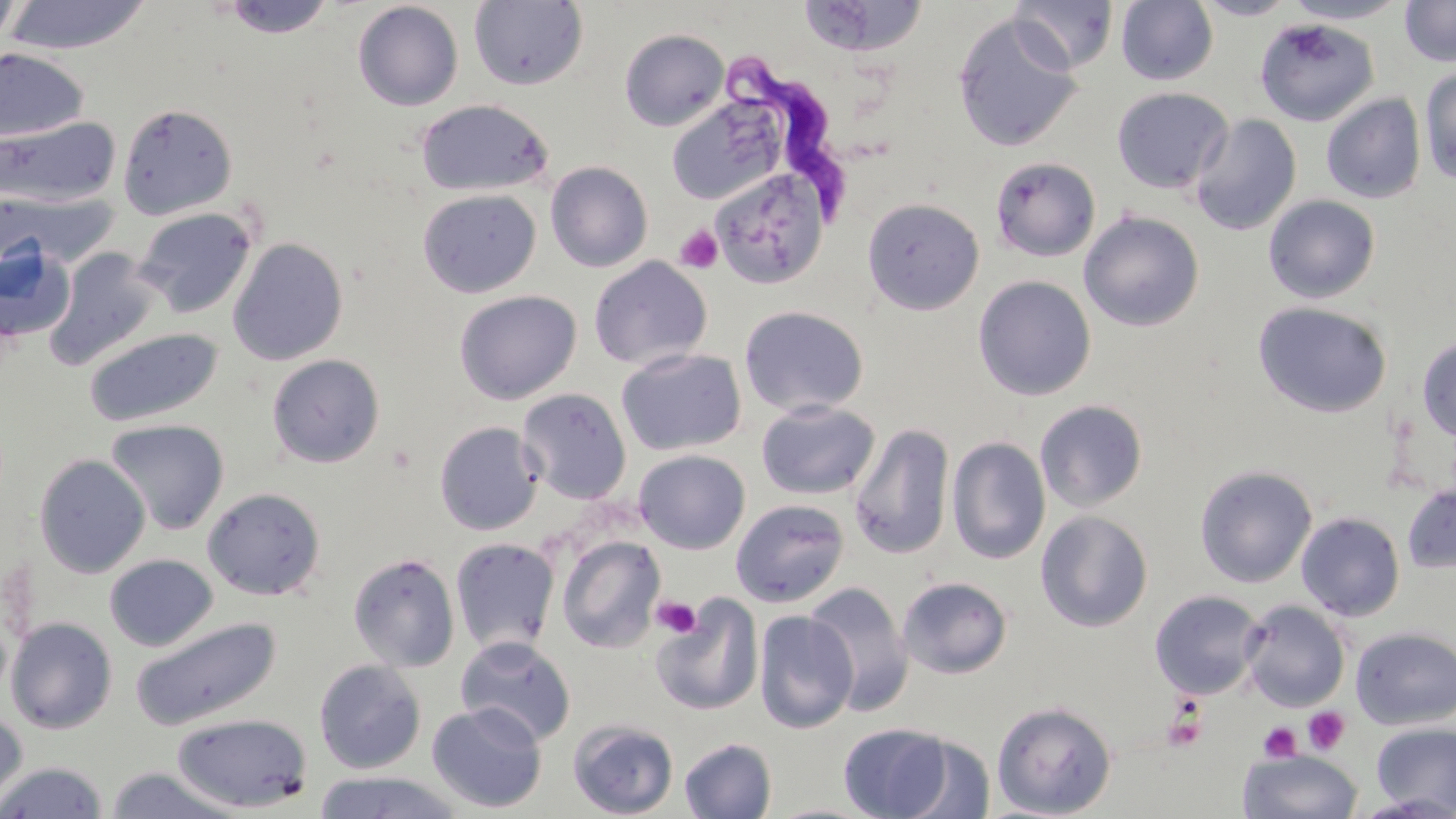
Summary:
  - Coordinate format: approximate bounding boxes as [x1, y1, x2, y2] in pixels
  - Platelet locations: [675, 225, 723, 273], [652, 595, 702, 638], [1161, 704, 1209, 754], [1304, 707, 1350, 754], [1258, 722, 1302, 763]
  - Uninfected red blood cell locations: [0, 0, 25, 53], [2, 0, 152, 55], [220, 0, 336, 38], [797, 0, 929, 58], [1009, 0, 1118, 74], [1116, 0, 1218, 85], [1194, 0, 1299, 20], [1285, 0, 1409, 24], [469, 1, 589, 91], [1400, 1, 1456, 67], [352, 2, 464, 111], [952, 12, 1084, 153], [1254, 18, 1379, 126], [619, 28, 729, 131], [0, 48, 89, 143], [1419, 66, 1456, 185], [1111, 86, 1234, 194], [665, 94, 789, 206], [1321, 94, 1425, 204], [416, 98, 554, 197], [117, 103, 238, 219], [1189, 114, 1302, 235], [0, 116, 121, 208], [990, 157, 1101, 262], [545, 161, 653, 272], [710, 168, 830, 289], [417, 188, 541, 297], [2, 191, 114, 267], [1263, 194, 1381, 304], [862, 198, 984, 315], [133, 206, 258, 319], [1079, 210, 1205, 332], [227, 237, 348, 366], [0, 241, 75, 344], [44, 247, 162, 370], [588, 256, 712, 371], [973, 275, 1096, 400], [453, 289, 581, 404], [1253, 301, 1392, 417], [738, 305, 868, 418], [83, 327, 224, 427], [1417, 335, 1456, 443], [616, 348, 746, 456], [266, 353, 385, 468], [517, 388, 632, 504], [1034, 399, 1148, 512], [756, 400, 880, 500], [105, 419, 229, 535], [434, 422, 543, 535], [849, 423, 955, 560], [947, 436, 1050, 565], [634, 450, 750, 554], [34, 453, 151, 579], [1194, 465, 1318, 588], [1401, 482, 1456, 574], [202, 486, 326, 601], [730, 499, 850, 607], [1035, 510, 1153, 631], [1296, 512, 1405, 621], [556, 535, 666, 653], [450, 537, 560, 656], [348, 552, 460, 672], [104, 554, 218, 651], [897, 576, 1013, 679], [803, 582, 914, 714], [1149, 589, 1265, 700], [650, 594, 764, 716], [1239, 600, 1350, 712], [754, 610, 858, 733], [4, 616, 118, 734], [130, 616, 282, 729], [1351, 626, 1456, 730], [455, 636, 576, 747], [313, 658, 426, 774], [991, 700, 1117, 818], [427, 702, 547, 814], [0, 706, 28, 816], [169, 713, 313, 812], [568, 719, 679, 818], [1371, 721, 1456, 816], [838, 722, 956, 818], [892, 733, 997, 819], [679, 738, 777, 819], [1238, 749, 1363, 819], [0, 761, 109, 818], [104, 766, 242, 818], [311, 770, 465, 818]
  - Trypanosoma brucei locations: [720, 53, 858, 223]
  - Slide-level diagnosis: Trypanosoma brucei
  - Magnification: 1000x
  - Stain: May-Grünwald-Giemsa
  - Preparation: thin blood smear
  - Field of view: single
  - Modality: optical microscopy
  - Image size: 1456×819 pixels